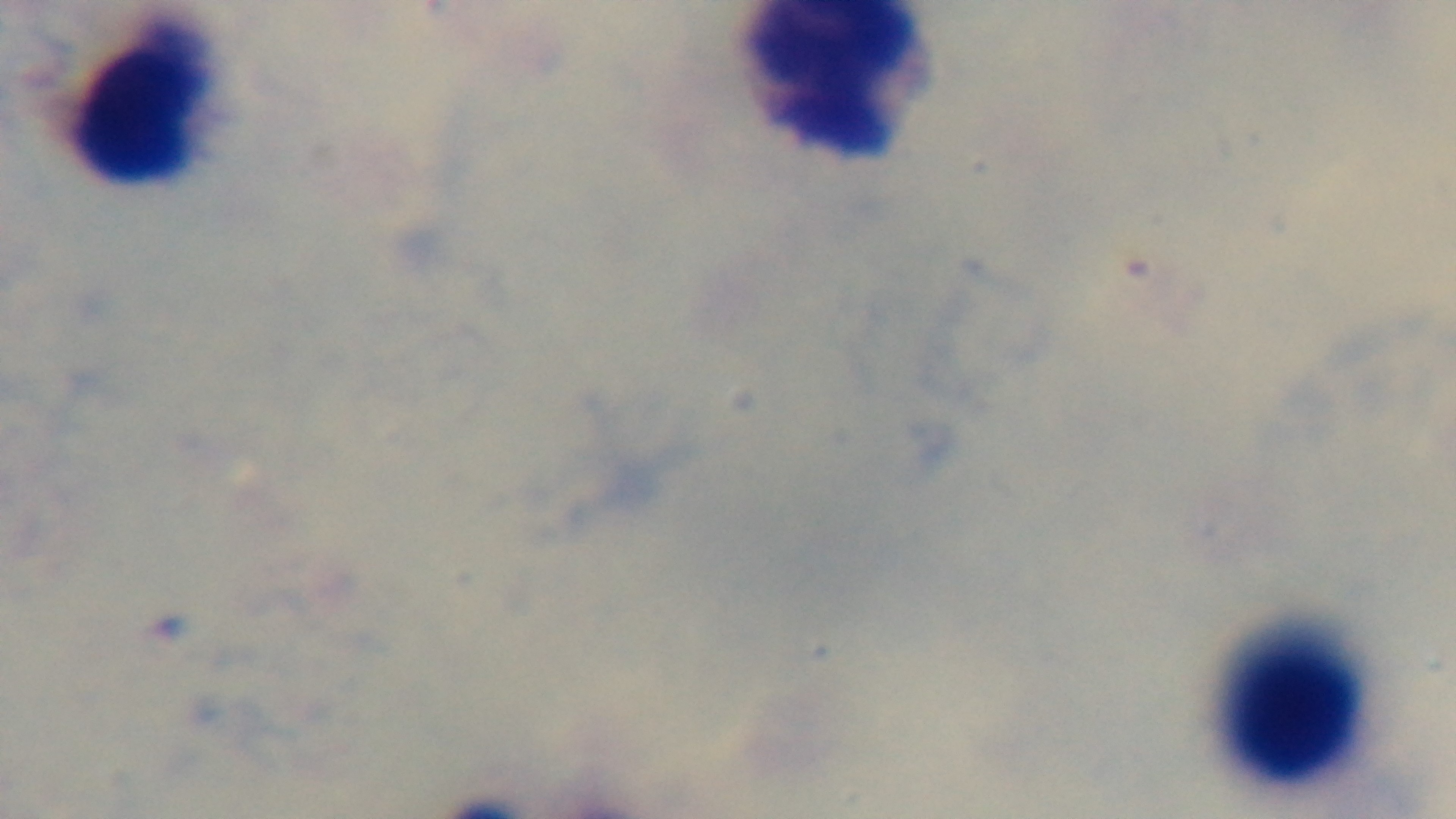
modality = light microscopy
capture = mounted 4K digital camera
malaria status = uninfected
objective = 100x oil immersion
preparation = thick smear
field of view = one from the slide
stain = Giemsa